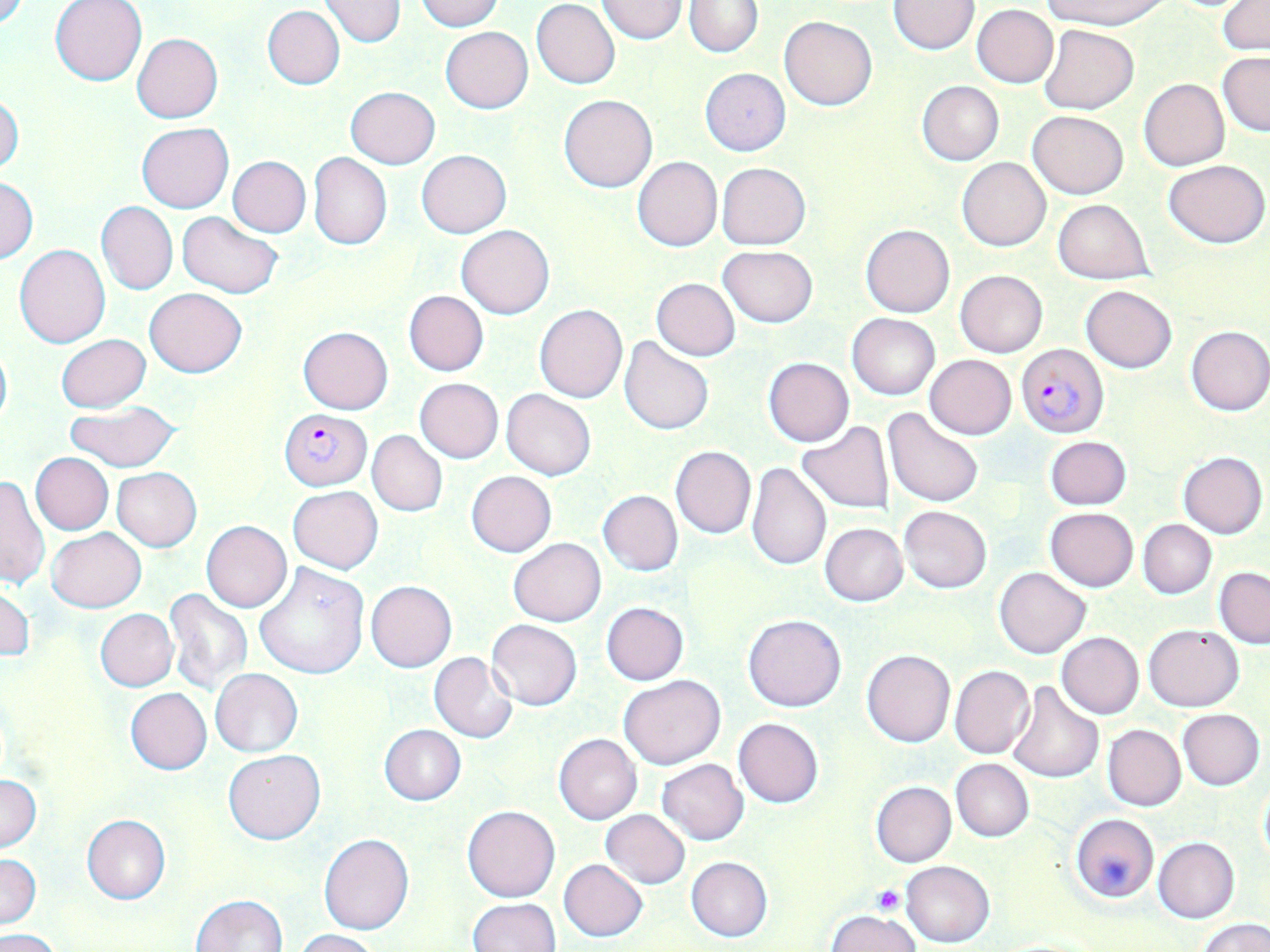
Summary:
  - Coordinate format: approximate bounding boxes as [x1, y1, x2, y2] in pixels
  - Uninfected red blood cell locations: [415, 0, 504, 31], [597, 0, 687, 44], [1037, 0, 1168, 29], [51, 1, 147, 85], [319, 1, 406, 47], [532, 1, 620, 88], [888, 1, 979, 54], [684, 2, 762, 57], [1218, 2, 1269, 55], [263, 5, 345, 89], [972, 5, 1058, 88], [780, 15, 877, 109], [1038, 24, 1139, 114], [440, 26, 533, 113], [132, 32, 223, 122], [1217, 52, 1270, 136], [700, 68, 790, 155], [1139, 78, 1229, 170], [917, 81, 1003, 165], [345, 86, 440, 168], [559, 94, 656, 192], [0, 95, 24, 176], [1026, 110, 1128, 199], [136, 122, 234, 213], [417, 150, 511, 237], [308, 152, 392, 250], [228, 156, 310, 237], [632, 156, 723, 251], [957, 157, 1050, 251], [1162, 159, 1269, 247], [717, 162, 810, 249], [1, 176, 37, 263], [1053, 199, 1153, 284], [97, 200, 177, 295], [176, 212, 283, 298], [861, 224, 954, 318], [457, 225, 553, 319], [15, 244, 109, 348], [719, 245, 817, 326], [955, 270, 1048, 357], [652, 278, 740, 361], [1082, 285, 1177, 373], [144, 288, 246, 377], [404, 291, 488, 376], [534, 304, 628, 403], [847, 312, 939, 400], [1185, 325, 1270, 416], [297, 326, 393, 414], [56, 334, 149, 412], [620, 338, 713, 435], [0, 341, 12, 432], [925, 354, 1016, 439], [762, 357, 854, 447], [414, 378, 503, 463], [502, 389, 595, 479], [64, 402, 181, 472], [883, 409, 982, 508], [795, 421, 896, 515], [368, 430, 447, 516], [1045, 436, 1131, 509], [670, 446, 756, 538], [680, 447, 811, 558], [1178, 451, 1267, 538], [30, 452, 113, 534], [746, 462, 831, 571], [112, 467, 202, 552], [466, 470, 556, 557], [0, 474, 49, 592], [288, 486, 383, 573], [598, 490, 683, 576], [898, 505, 991, 593], [1045, 508, 1138, 592], [1139, 520, 1216, 598], [201, 521, 292, 612], [820, 523, 908, 606], [47, 527, 145, 611], [508, 538, 606, 626], [253, 564, 370, 681], [1214, 566, 1270, 648], [994, 567, 1091, 659], [366, 581, 457, 672], [0, 584, 33, 666], [163, 589, 255, 695], [601, 602, 689, 685], [95, 608, 178, 692], [743, 614, 846, 712], [487, 619, 582, 710], [1143, 623, 1244, 711], [1056, 632, 1144, 718], [862, 649, 955, 747], [429, 652, 517, 743], [949, 665, 1034, 759], [211, 668, 302, 757], [619, 675, 725, 769], [1006, 682, 1105, 784], [126, 688, 212, 774], [1177, 709, 1265, 790], [733, 717, 823, 807], [1103, 723, 1186, 811], [380, 725, 465, 805], [553, 734, 642, 825], [224, 749, 325, 845], [657, 758, 749, 845], [950, 758, 1034, 841], [0, 776, 41, 851], [1258, 779, 1270, 868], [871, 781, 955, 867], [463, 806, 560, 902], [601, 810, 689, 889], [1070, 813, 1159, 904], [82, 814, 171, 905], [319, 834, 415, 935], [1153, 836, 1239, 923], [0, 854, 42, 930], [686, 857, 773, 942], [559, 858, 647, 941], [901, 860, 995, 947], [190, 895, 288, 952], [468, 898, 559, 951], [826, 909, 923, 952], [1196, 918, 1269, 952], [1, 929, 65, 952], [295, 929, 380, 952]
  - Plasmodium falciparum-infected red blood cell locations: [1017, 343, 1108, 437], [280, 408, 371, 489]
  - Platelet locations: [871, 884, 905, 915]
  - Slide-level diagnosis: Plasmodium falciparum
  - Preparation: thin blood film
  - Modality: optical microscopy
  - Stain: May-Grünwald-Giemsa
  - Field of view: single
  - Magnification: 1000x
  - Image size: 1270×952 pixels